Report the malaria status of this cell.
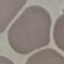

It is uninfected.

Summary:
  - Preparation: thin blood smear
  - Capture: smartphone through the microscope eyepiece
  - Stain: Giemsa
  - Image type: cell patch, automatically extracted from a larger field of view and resized to 64 × 64 pixels